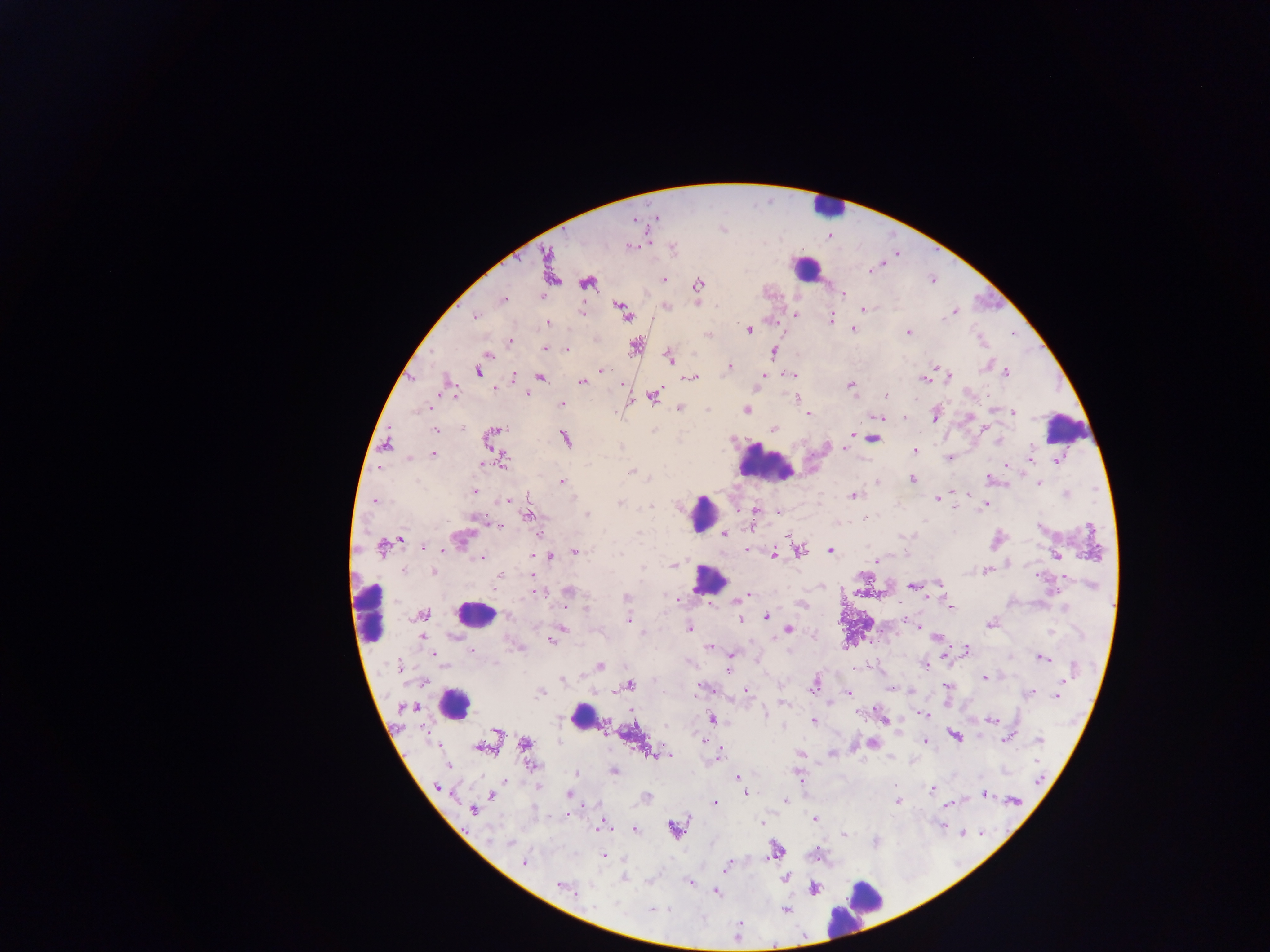

Approximate centers as x y in pixels.
Summary:
  - Malaria parasite locations: 656 217; 633 220; 630 246; 673 248; 871 270; 551 273; 663 279; 587 282; 698 284; 843 294; 504 300; 623 308; 865 309; 581 312; 953 312; 796 315; 475 317; 946 317; 831 318; 548 323; 748 330; 853 330; 908 333; 708 335; 509 341; 636 344; 545 349; 567 350; 773 351; 487 355; 669 358; 730 367; 604 370; 478 372; 1005 373; 790 375; 514 376; 763 376; 949 376; 541 377; 691 379; 924 379; 582 381; 448 382; 850 385; 494 388; 527 394; 453 395; 885 396; 654 397; 796 397; 562 404; 428 408; 680 408; 747 410; 1013 412; 808 414; 935 415; 877 417; 904 418; 463 428; 435 429; 497 429; 774 429; 853 434; 492 436; 565 438; 873 438; 997 439; 385 443; 845 447; 915 450; 434 454; 1030 457; 409 458; 503 459; 1057 460; 1007 464; 481 465; 631 472; 987 478; 912 479; 877 481; 561 482; 1039 483; 475 492; 1066 494; 854 496; 938 498; 375 500; 509 500; 620 503; 986 504; 650 506; 755 510; 587 514; 529 516; 478 518; 499 525; 1091 531; 725 532; 538 534; 401 539; 382 547; 424 547; 748 550; 799 550; 830 550; 575 552; 774 554; 533 556; 1056 556; 551 557; 482 558; 877 561; 674 565; 433 571; 986 571; 500 576; 940 584; 912 586; 568 591; 540 592; 746 596; 626 597; 676 598; 741 598; 951 607; 585 609; 424 614; 767 617; 628 620; 740 620; 989 624; 919 626; 560 629; 688 629; 789 629; 643 632; 422 637; 938 638; 552 640; 709 647; 966 648; 471 651; 434 654; 731 654; 1042 658; 925 665; 399 666; 600 666; 729 671; 985 677; 562 680; 1062 682; 815 684; 630 685; 947 685; 700 689; 746 691; 1031 692; 540 693; 848 693; 1057 695; 783 703; 409 706; 764 713; 923 714; 712 720; 991 720; 813 721; 886 722; 497 731; 954 735; 1007 738; 1039 740; 703 742; 925 742; 525 743; 872 744; 480 748; 719 752; 799 753; 831 753; 651 754; 667 755; 447 765; 531 766; 614 770; 576 773; 737 777; 1040 778; 895 785; 437 787; 538 788; 932 789; 742 790; 745 794; 491 795; 569 795; 984 795; 647 796; 785 801; 898 801; 1015 801; 715 802; 949 804; 473 811; 815 819; 761 822; 941 826; 602 827; 635 829; 674 829; 963 834; 844 835; 510 843; 775 850; 603 855; 524 862; 728 865; 624 878; 784 878; 690 883; 561 886; 814 888; 716 893; 616 904; 594 906; 651 910; 786 910
  - Leukocyte locations: 828 207; 804 268; 1067 425; 765 463; 704 513; 708 580; 369 611; 475 614; 455 704; 583 717; 861 904
  - Country: Ghana
  - Field of view: single
  - Preparation: thick blood film
  - Image size: 1270×952 pixels
  - Capture: mobile-phone photograph through a microscope